Give the position of every Plasmodium parasite visible.
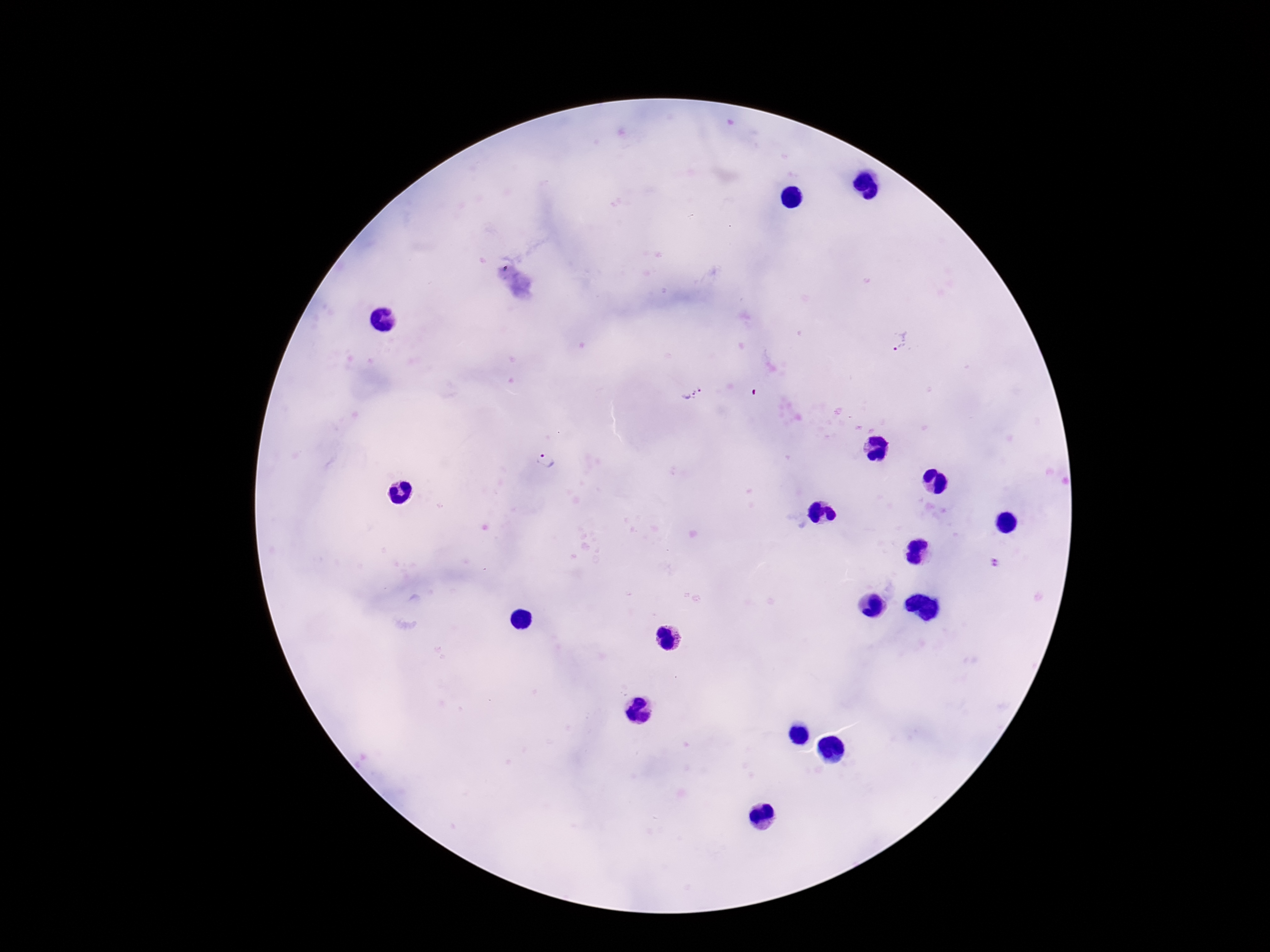

Approximate centers as [x, y] in pixels.
Plasmodium parasites: [900, 342], [692, 394], [545, 461].

Giemsa-stained preparation. One field from this slide. 100x magnification. Photographed through the microscope eyepiece with a smartphone camera. Thick blood film. Image is 1270×952 pixels. Patient malaria status: infected.